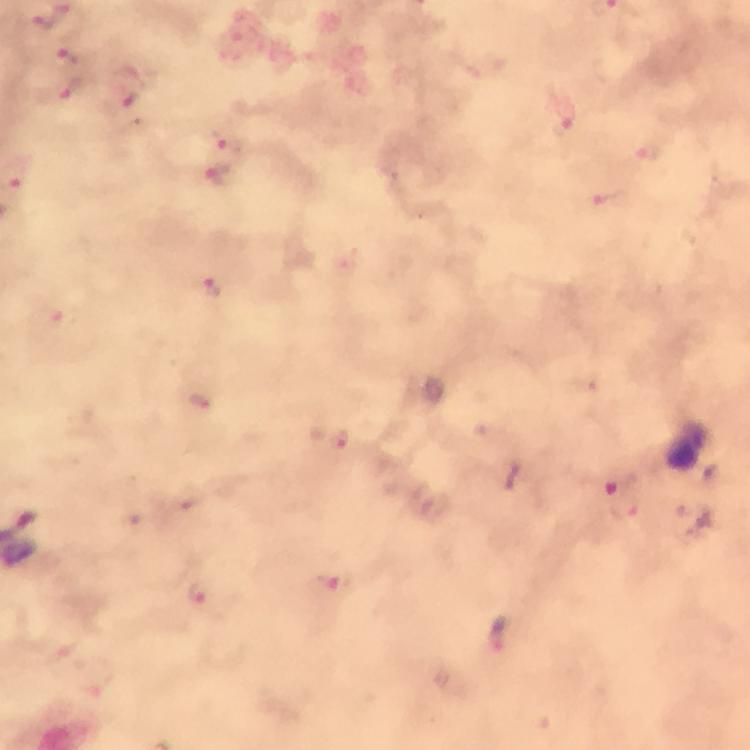 Approximate centers as {x, y} in pixels. Malaria parasite locations: {73, 58}, {72, 91}, {126, 100}, {564, 127}, {226, 140}, {221, 178}, {214, 287}, {200, 402}, {341, 439}, {621, 484}, {627, 509}, {335, 584}, {200, 595}, {502, 633}. Immersion oil was used. At 100x magnification. Image is 750×750 pixels. From a diagnostic examination for malaria. Photographed with a smartphone mounted on the microscope. Thick blood film. Cropped region of a single field of view. Giemsa stain.